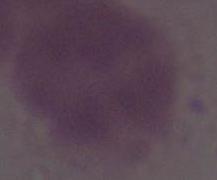
Summary:
  - Identification: red blood cell
  - Magnification: 1000x
  - Modality: photomicrograph